Identify the parasite.
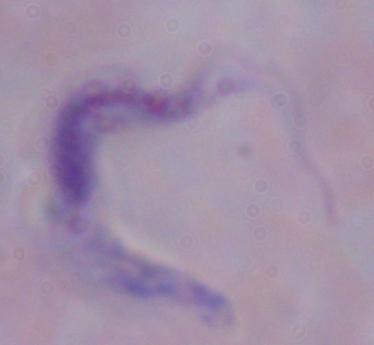
This is a trypanosome.

Summary:
  - Magnification: 1000x
  - Modality: micrograph